Assess this cell for malaria.
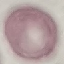

It is uninfected.

Acquired by smartphone through the microscope eyepiece. Giemsa stain. Thin blood film. Cell patch, automatically extracted from a larger field of view and resized to 64 × 64 pixels.